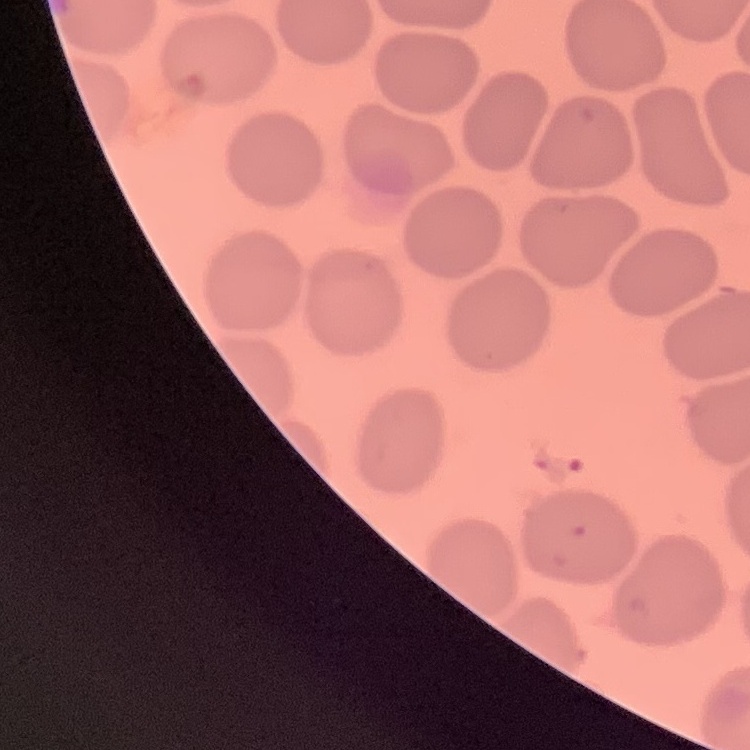
red_blood_cell_morphology: no rouleaux formation
preparation: thin blood film
image_type: one tile cut from a larger photomicrograph
stain: Field's or Giemsa